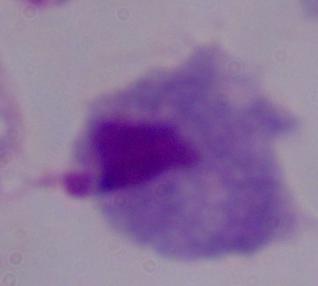
Captured at 1000x magnification. Micrograph. A trichomonad is shown.